State the blood parasite species.
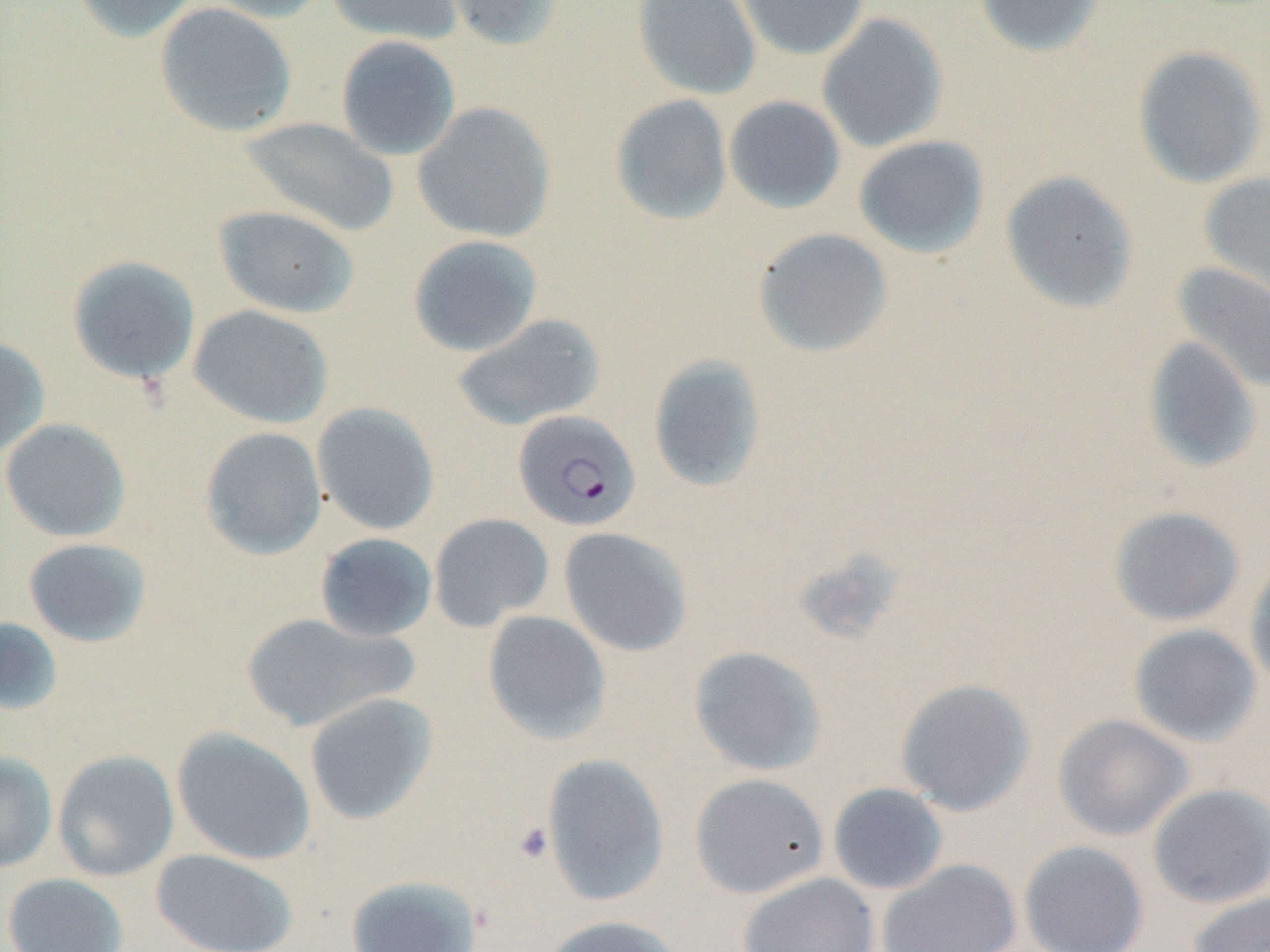
Plasmodium falciparum.

Summary:
  - Coordinate format: approximate bounding boxes as [x1, y1, x2, y2] in pixels
  - Platelet locations: [513, 821, 554, 864]
  - Plasmodium falciparum-infected red blood cell locations: [513, 410, 641, 532]
  - Uninfected red blood cell locations: [72, 0, 201, 43], [194, 0, 328, 23], [324, 0, 463, 45], [438, 0, 564, 52], [632, 0, 761, 101], [735, 0, 870, 60], [973, 0, 1107, 57], [154, 2, 298, 138], [816, 12, 948, 153], [336, 35, 462, 161], [1132, 44, 1269, 189], [610, 94, 733, 225], [723, 95, 846, 214], [412, 101, 557, 243], [240, 117, 399, 237], [853, 134, 990, 259], [1000, 169, 1139, 314], [1199, 172, 1270, 304], [213, 205, 360, 319], [753, 227, 893, 358], [407, 235, 543, 357], [67, 255, 201, 385], [1171, 262, 1270, 392], [188, 305, 334, 429], [451, 313, 606, 432], [0, 335, 51, 458], [1141, 335, 1263, 474], [648, 355, 767, 493], [312, 402, 440, 536], [0, 418, 132, 542], [200, 426, 328, 560], [1108, 505, 1245, 626], [428, 512, 554, 631], [558, 527, 693, 656], [314, 532, 437, 642], [23, 537, 153, 647], [1245, 556, 1270, 695], [240, 611, 415, 732], [482, 611, 612, 745], [0, 617, 64, 715], [1128, 623, 1262, 747], [689, 646, 827, 776], [894, 678, 1036, 816], [303, 692, 439, 825], [1053, 714, 1194, 841], [171, 727, 316, 865], [52, 749, 179, 881], [0, 751, 58, 873], [541, 754, 670, 906], [690, 773, 829, 898], [828, 783, 948, 895], [1147, 783, 1270, 908], [1019, 841, 1149, 952], [150, 848, 299, 952], [877, 858, 1021, 951], [739, 871, 879, 952], [2, 872, 129, 952], [345, 873, 483, 952], [1187, 892, 1270, 952], [539, 915, 687, 952]
  - Image size: 1270×952 pixels
  - Preparation: thin blood smear
  - Modality: optical microscopy
  - Field of view: single
  - Magnification: 1000x
  - Stain: May-Grünwald-Giemsa